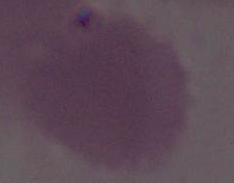

Summary:
  - Identification: red blood cell
  - Magnification: 1000x
  - Modality: photomicrograph